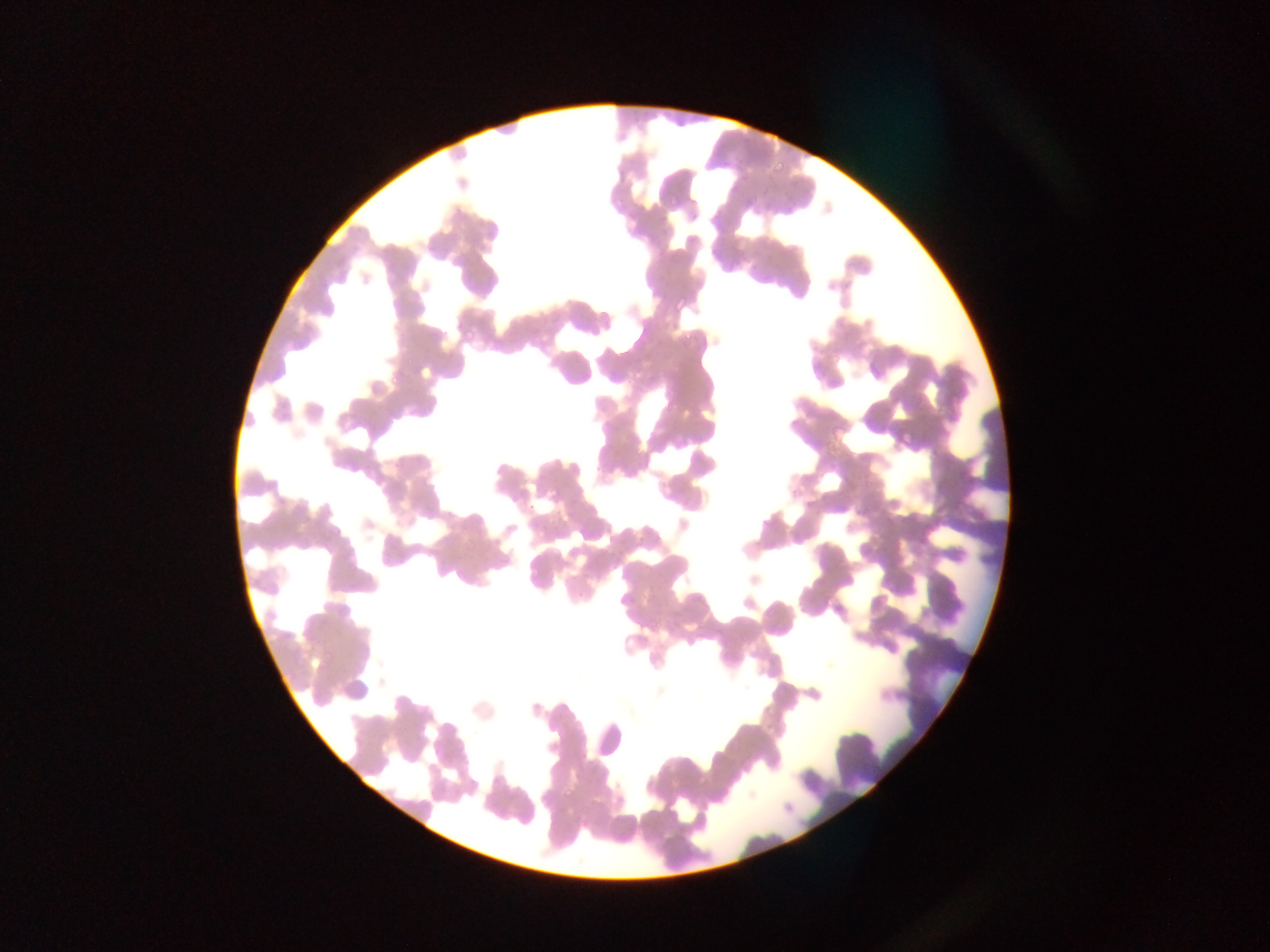

Approximate bounding boxes as (left, top, right, bottom) in pixels. Malaria parasite locations: (772, 160, 785, 172), (788, 180, 796, 186), (669, 193, 682, 206), (744, 195, 754, 205), (616, 198, 623, 208), (764, 202, 772, 210), (786, 204, 793, 215), (690, 207, 704, 222), (715, 209, 722, 217), (663, 225, 668, 235), (677, 297, 687, 310), (464, 329, 475, 340), (684, 329, 695, 340), (388, 374, 399, 383), (898, 432, 913, 445), (465, 540, 475, 549), (565, 788, 574, 798) | approximate (x, y) pixel centers of objects too small to bound: (743, 177). Sample from Ghana. Thin blood smear. Image is 1270×952 pixels. Single field of view. Photographed through a microscope with a mobile-phone camera.